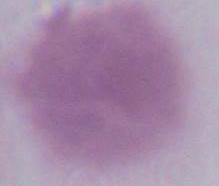
magnification = 1000x
modality = micrograph
identification = red blood cell